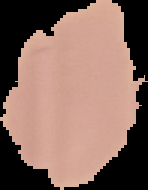 The area outside the segmented cell region is set to black. Malaria status: uninfected. Image is 148×190 pixels. From a thin blood film.